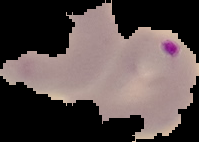
preparation = thin blood film
result = Plasmodium parasites identified
image size = 199×142 pixels
image type = segmented cell region with the area outside set to black